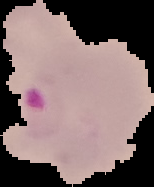

image type = cell region segmented out of the field of view; surrounding area masked to black
preparation = thin blood smear
malaria status = parasitized
image size = 154×187 pixels